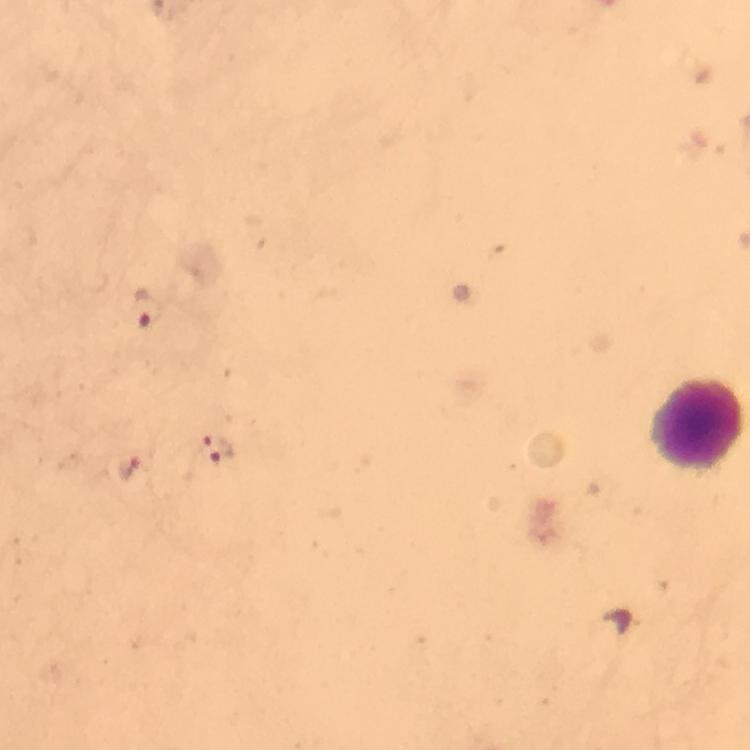

Approximate centers as (x, y) in pixels.
Summary:
  - Leukocyte locations: (696, 425)
  - Malaria parasite locations: (146, 309), (220, 452), (129, 469)
  - Immersion oil: used
  - Magnification: 100x
  - Context: from a diagnostic examination for malaria
  - Cropped from: a single field of view
  - Preparation: thick blood film
  - Stain: Giemsa
  - Image size: 750×750 pixels
  - Capture: smartphone mounted on the microscope